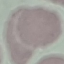
Result: no malaria parasites seen. Giemsa stain. Automatically extracted cell patch, resized to 64 × 64 pixels. Thin blood film. Acquired by smartphone through the microscope eyepiece.